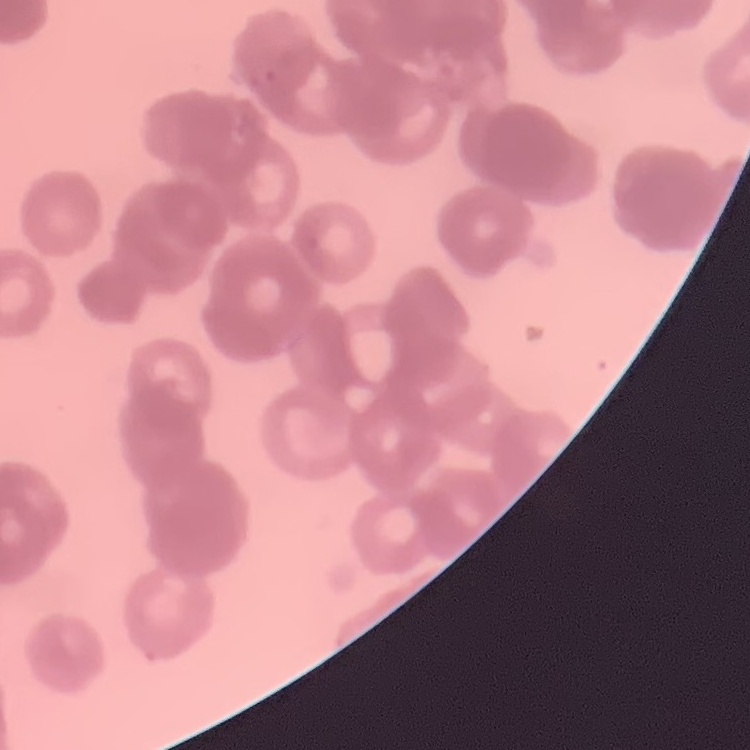

red blood cell morphology = rouleaux formation
stain = Field's or Giemsa
preparation = thin peripheral smear
image type = square crop of a larger photomicrograph